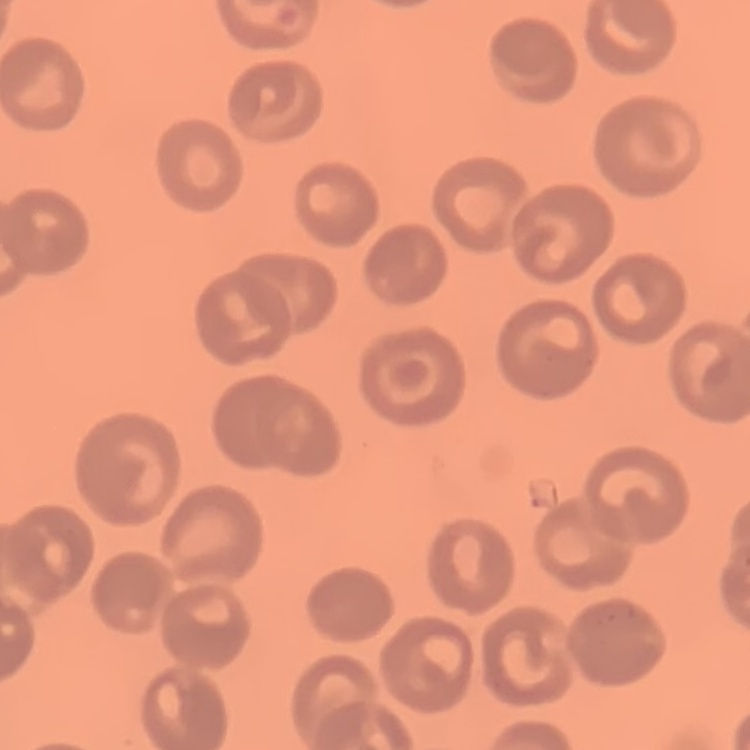

Summary:
  - Erythrocyte morphology: no rouleaux formation
  - Stain: Field's or Giemsa
  - Preparation: thin blood smear
  - Image type: square crop of a larger photomicrograph